Mark where platelets are.
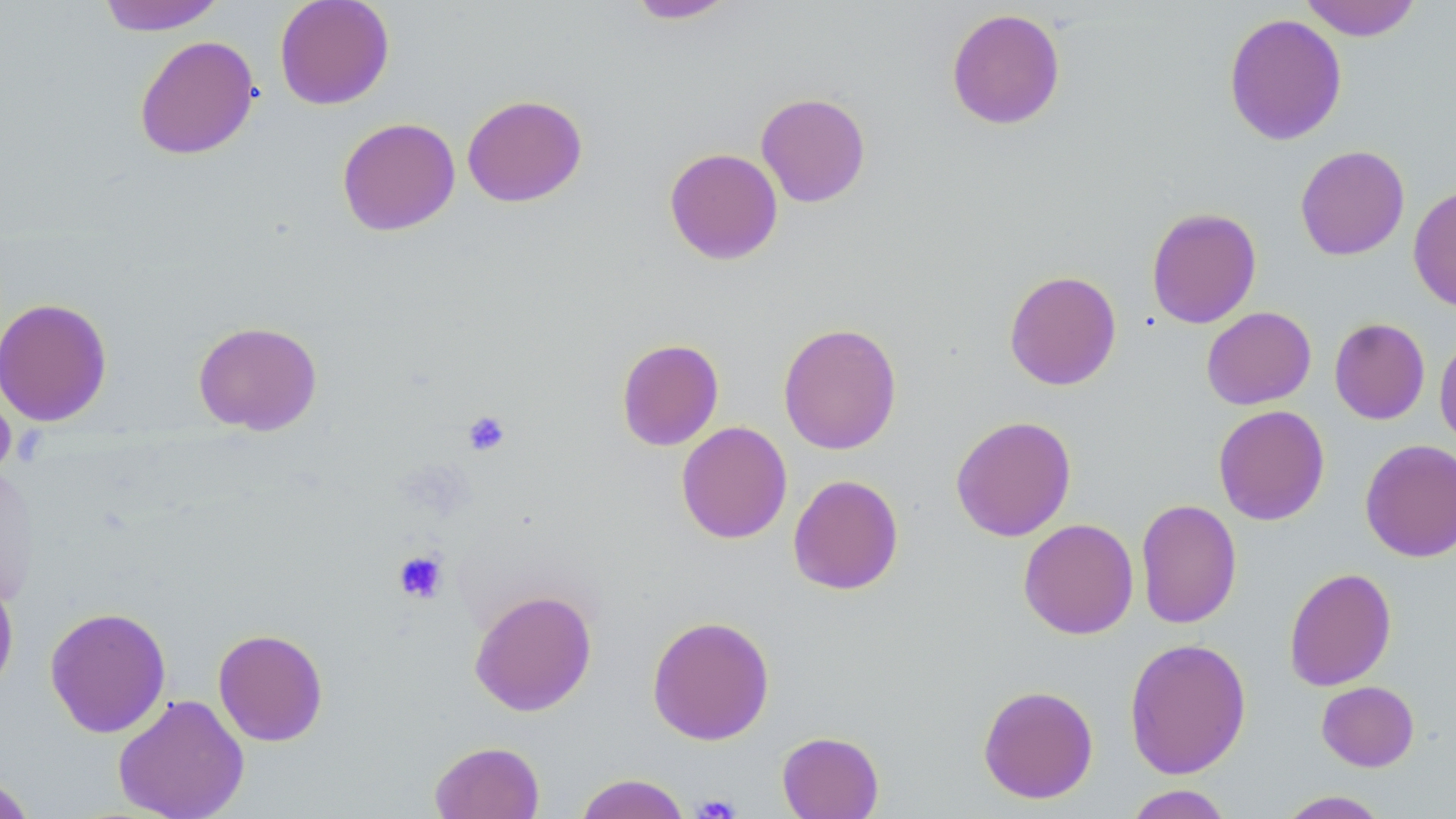

Approximate bounding boxes as (x1, y1, x2, y2) in pixels.
Platelets: (462, 411, 511, 456), (393, 549, 449, 604), (691, 793, 741, 819).

{
  "slide_level_diagnosis": "negative for blood parasites",
  "uninfected_red_blood_cell_locations": "approximate bounding boxes as (x1, y1, x2, y2) in pixels: (96, 0, 227, 35), (273, 0, 395, 110), (625, 0, 739, 24), (1298, 0, 1423, 41), (946, 7, 1066, 130), (1223, 12, 1347, 146), (134, 35, 260, 160), (756, 92, 871, 207), (461, 94, 587, 207), (337, 117, 460, 236), (1295, 145, 1410, 260), (664, 147, 783, 265), (1408, 185, 1456, 313), (1146, 207, 1262, 329), (1004, 270, 1122, 390), (0, 297, 113, 426), (1201, 306, 1316, 410), (1329, 317, 1430, 424), (193, 320, 323, 435), (778, 322, 902, 455), (1434, 331, 1456, 449), (616, 338, 724, 451), (0, 379, 17, 486), (1213, 405, 1330, 526), (950, 415, 1076, 542), (676, 421, 793, 544), (1360, 439, 1456, 562), (0, 463, 40, 607), (787, 474, 904, 595), (1135, 498, 1242, 629), (1018, 518, 1139, 639), (1283, 567, 1397, 691), (0, 569, 19, 697), (469, 588, 598, 716), (44, 606, 172, 738), (647, 615, 775, 746), (213, 628, 328, 746), (1124, 637, 1252, 779), (1316, 680, 1420, 771), (978, 684, 1099, 804), (113, 693, 250, 819), (777, 731, 884, 819), (429, 740, 545, 819), (0, 773, 38, 818), (574, 773, 691, 819), (1122, 784, 1236, 819), (1275, 790, 1392, 818)",
  "field_of_view": "one of a larger specimen",
  "preparation": "thin blood smear",
  "image_size": "1456×819 pixels",
  "magnification": "1000x",
  "modality": "light microscopy",
  "stain": "May-Grünwald-Giemsa"
}